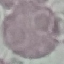
Result: no malaria parasites detected. Acquired by smartphone through the microscope eyepiece. Thin smear of blood. Automatically extracted cell patch, resized to 64 × 64 pixels. Giemsa-stained preparation.